Classify this cell by malaria status.
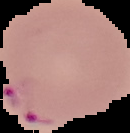
It is parasitized.

From a thin blood smear. Image is 130×133 pixels. Segmented cell region on a black background.